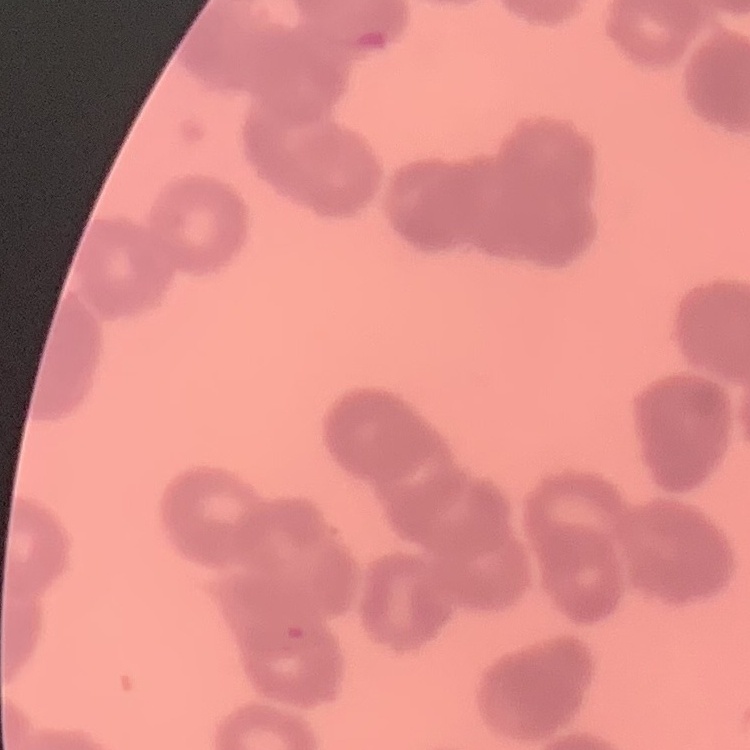
The red blood cells exhibit rouleaux formation. Thin peripheral smear. Field's or Giemsa stain. One tile cut from a larger photomicrograph.